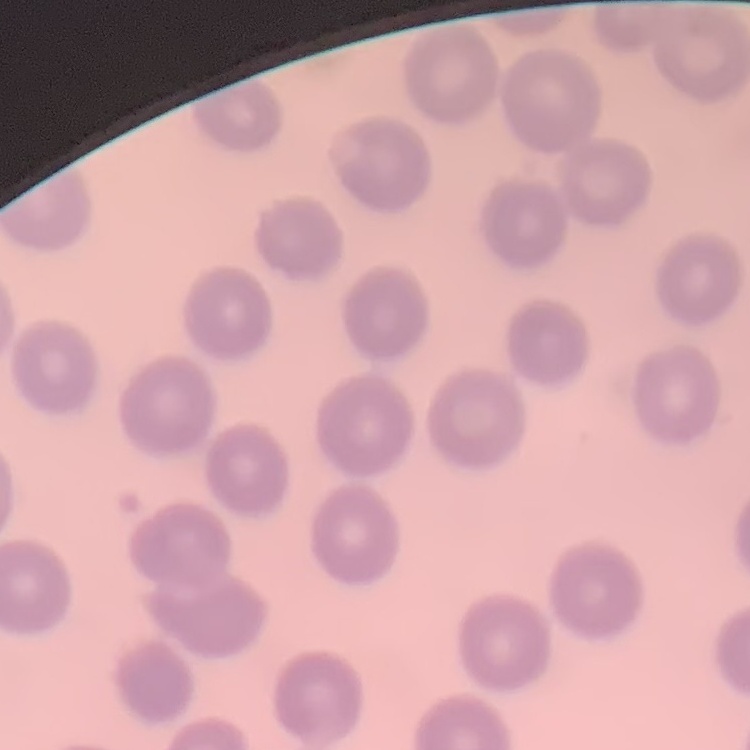

erythrocyte morphology = no rouleaux formation
image type = square crop of a larger photomicrograph
preparation = thin peripheral smear
stain = Field's or Giemsa